Give the preparation type.
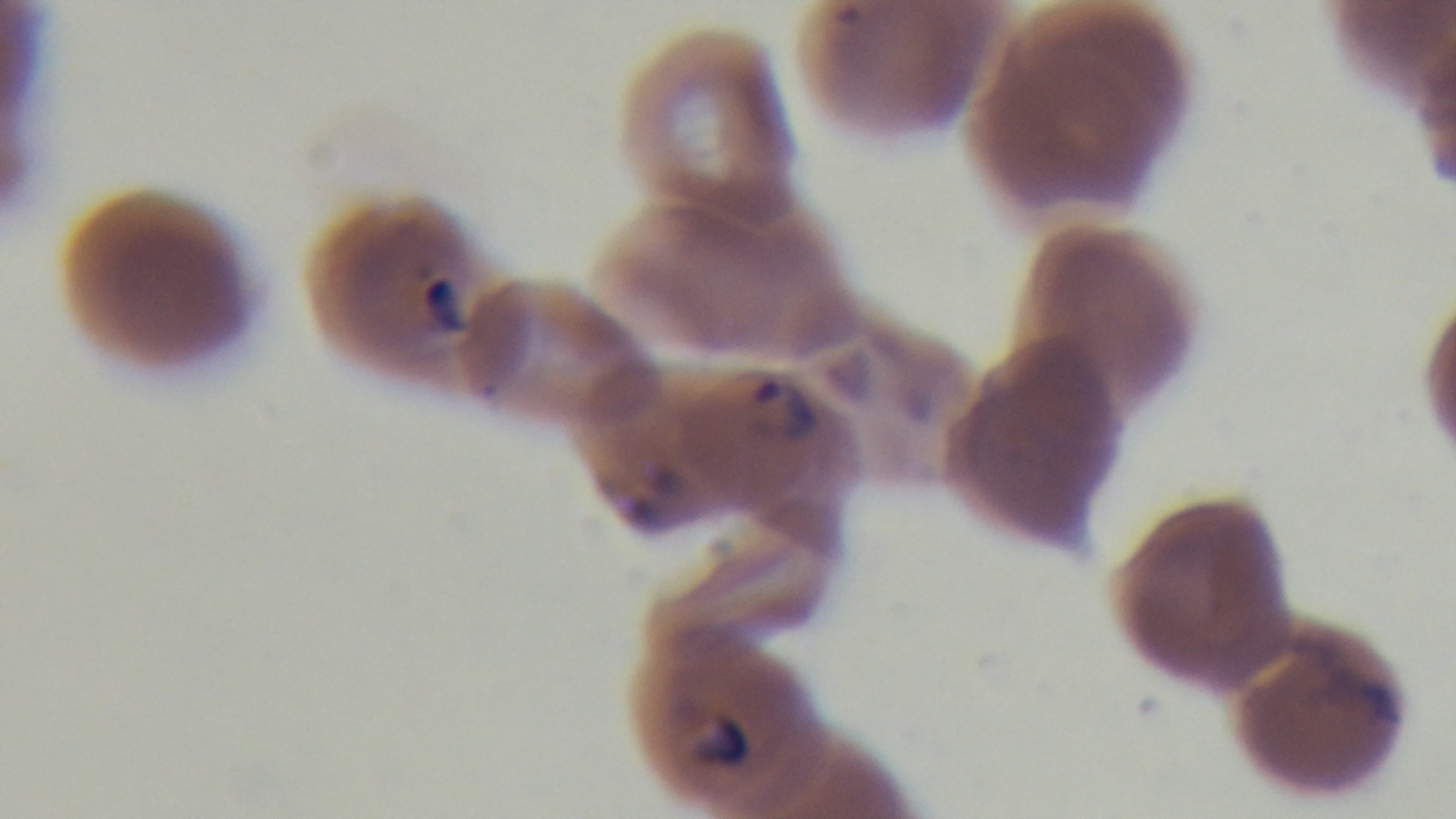
Thin.

field of view = single
objective = 100x oil immersion
capture = mounted 4K digital camera
stain = Giemsa
modality = light microscopy
malaria status = positive